Report the malaria status of this cell.
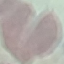

It is uninfected.

Summary:
  - Image type: automatically extracted cell patch, resized to 64 × 64 pixels
  - Capture: smartphone through the microscope eyepiece
  - Stain: Giemsa
  - Preparation: thin blood film